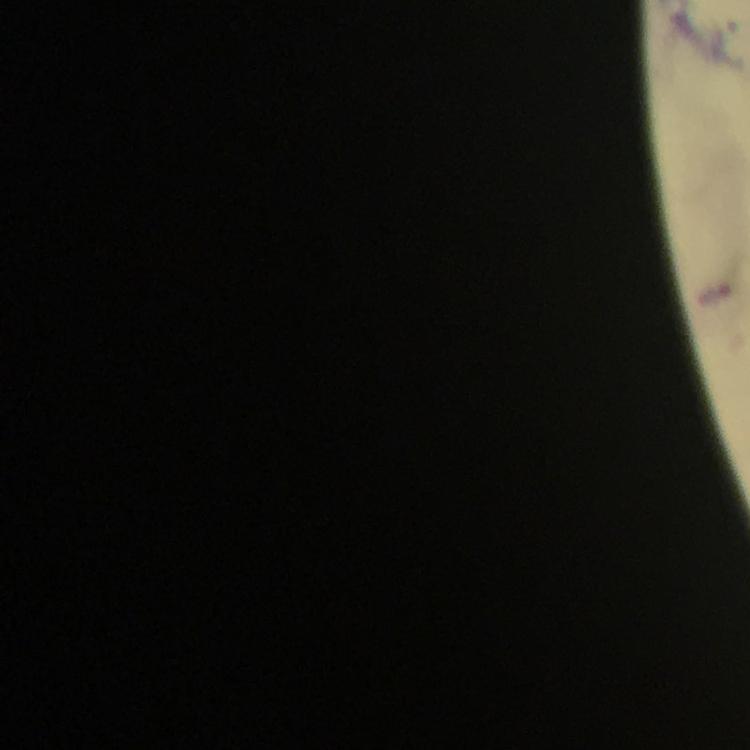

Approximate object centers, in pixels from the top-left corner. Malaria parasite locations: (x=715, y=294). From a malaria diagnostic workup. Immersion oil was used. Thick blood film. Photographed with a smartphone mounted on the microscope. Giemsa stain. A crop from one field of view. Image is 750×750 pixels. At 100x magnification.